Report the malaria status of this cell.
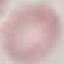

It is uninfected.

capture = smartphone through the microscope eyepiece
stain = Giemsa
image type = automatically extracted cell patch, resized to 64 × 64 pixels
preparation = thin blood smear